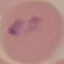
Malaria status: uninfected. Automatically extracted cell patch, resized to 64 × 64 pixels. Giemsa stain. Acquired by smartphone through the microscope eyepiece. Thin smear of blood.